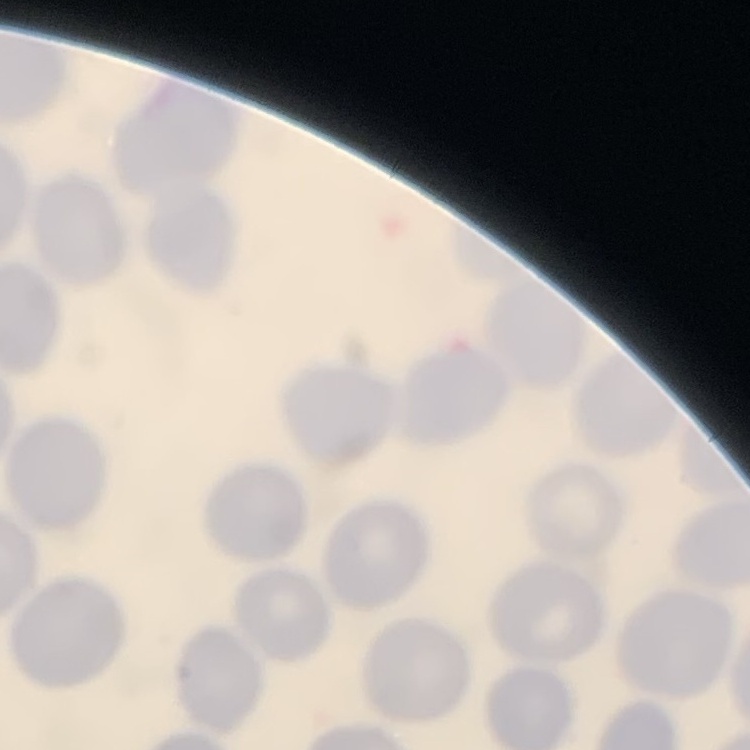

red blood cell morphology = no rouleaux formation
image type = one tile cut from a larger photomicrograph
preparation = thin peripheral smear
stain = Field's or Giemsa